Give the position of every Plasmodium parasite.
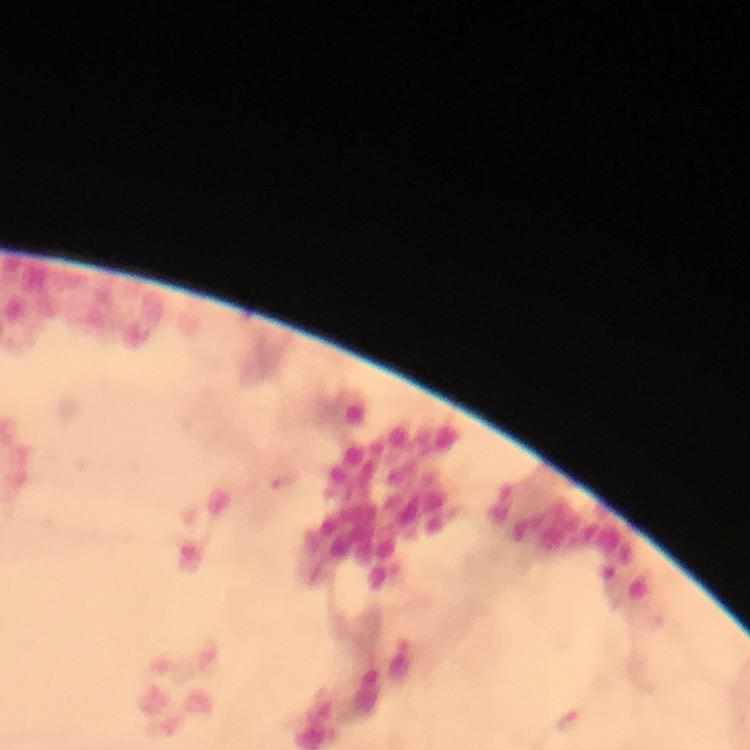
Approximate centers as {x, y} in pixels.
Plasmodium parasites: {280, 478}, {570, 720}.

Summary:
  - Cropped from: a single field of view
  - Preparation: thick blood smear
  - Capture: smartphone photograph through a microscope
  - Magnification: 100x
  - Immersion oil: applied
  - Image size: 750×750 pixels
  - Stain: Giemsa
  - Context: from a malaria diagnostic workup